Classify this cell by malaria status.
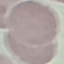
Uninfected.

Thin smear of blood. Giemsa stain. Photographed with a smartphone camera at the microscope eyepiece. Cell patch, automatically extracted from a larger field of view and resized to 64 × 64 pixels.